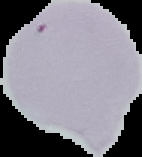

image_size: 142×157 pixels
image_type: segmented cell region on a black background
preparation: thin blood smear
malaria_status: uninfected